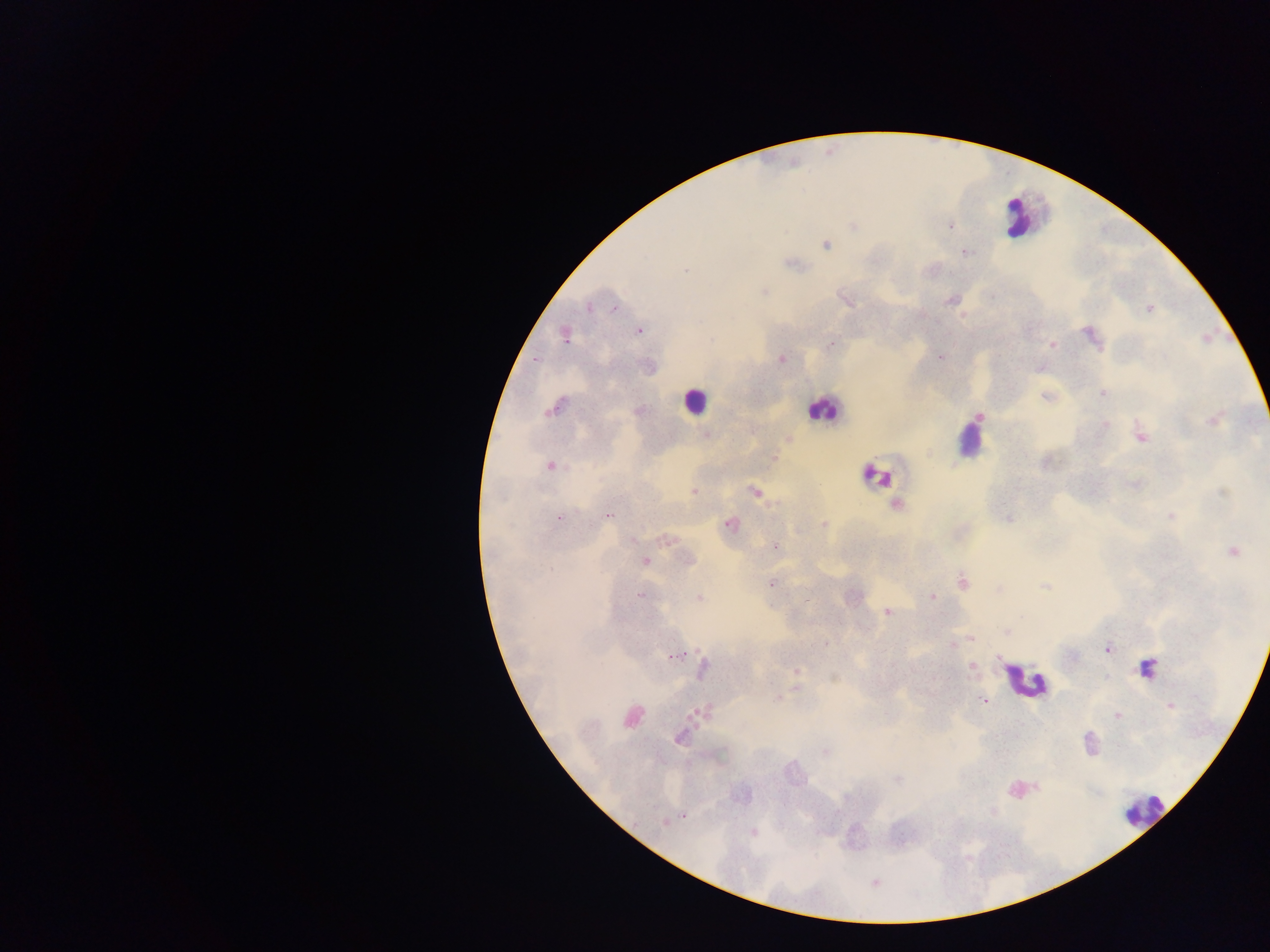
Approximate centers as (x, y) in pixels.
Summary:
  - Plasmodium parasite locations: (853, 226), (951, 226), (1009, 235), (828, 245), (967, 252), (791, 264), (686, 271), (766, 291), (842, 296), (949, 301), (848, 303), (614, 306), (591, 307), (1148, 309), (639, 330), (1086, 331), (563, 335), (710, 340), (831, 343), (1051, 344), (1097, 346), (941, 356), (782, 360), (536, 364), (1101, 393), (1043, 396), (555, 407), (978, 416), (1212, 420), (1105, 425), (1140, 435), (787, 440), (930, 454), (774, 455), (1044, 463), (550, 466), (871, 475), (881, 479), (1223, 490), (693, 491), (754, 491), (896, 504), (1170, 515), (607, 516), (1008, 518), (560, 519), (731, 523), (823, 523), (666, 542), (774, 546), (1232, 550), (644, 561), (688, 562), (961, 580), (771, 582), (1044, 585), (998, 589), (638, 595), (850, 597), (932, 597), (700, 598), (885, 613), (1005, 631), (971, 637), (826, 642), (953, 646), (1106, 648), (670, 657), (971, 666), (1148, 668), (796, 670), (703, 672), (834, 678), (797, 687), (778, 696), (984, 701), (1170, 706), (697, 712), (1118, 717), (677, 742), (824, 752), (896, 780), (1035, 787), (1016, 790), (993, 811), (686, 814), (663, 825), (754, 834), (910, 841)
  - Leukocyte locations: (698, 402), (823, 411), (1028, 679)
  - Country: Ghana
  - Image size: 1270×952 pixels
  - Preparation: thick blood film
  - Field of view: single
  - Capture: mobile-phone photograph through a microscope